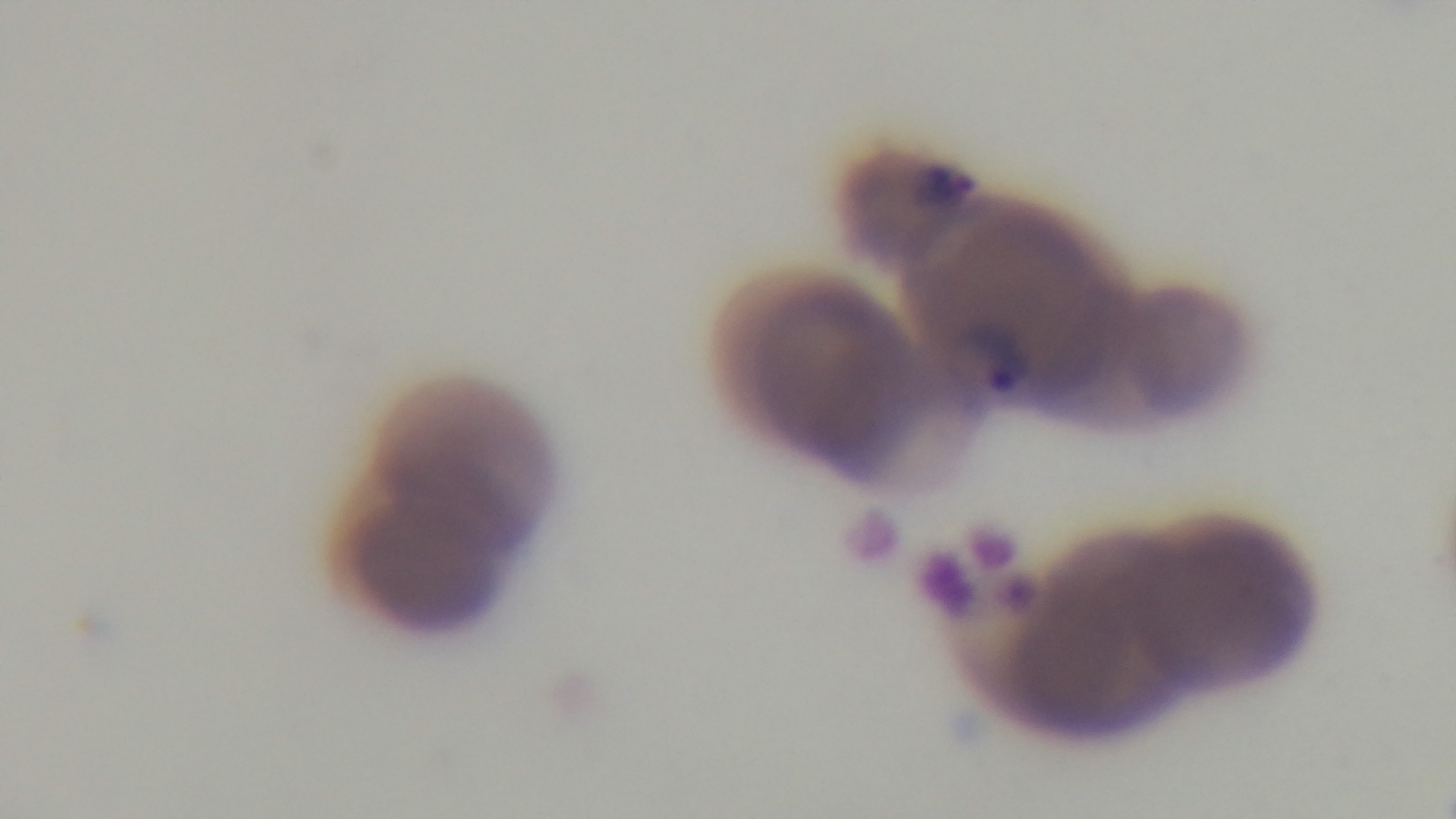
Summary:
  - Malaria status: positive
  - Field of view: one from the slide
  - Preparation: thin smear
  - Capture: mounted 4K digital camera
  - Objective: 100x oil immersion
  - Modality: light microscopy
  - Stain: Giemsa